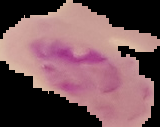
Summary:
  - Preparation: thin blood film
  - Result: Plasmodium parasites identified
  - Image type: segmented cell region with the area outside set to black
  - Image size: 160×127 pixels